Report the malaria status of this cell.
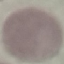
It is uninfected.

Cell patch, automatically extracted from a larger field of view and resized to 64 × 64 pixels. Giemsa stain. Thin blood smear. Photographed with a smartphone camera at the microscope eyepiece.